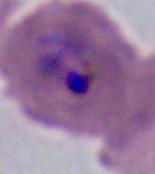

A Plasmodium parasite is shown. 400x or 1000x magnification. Photomicrograph.